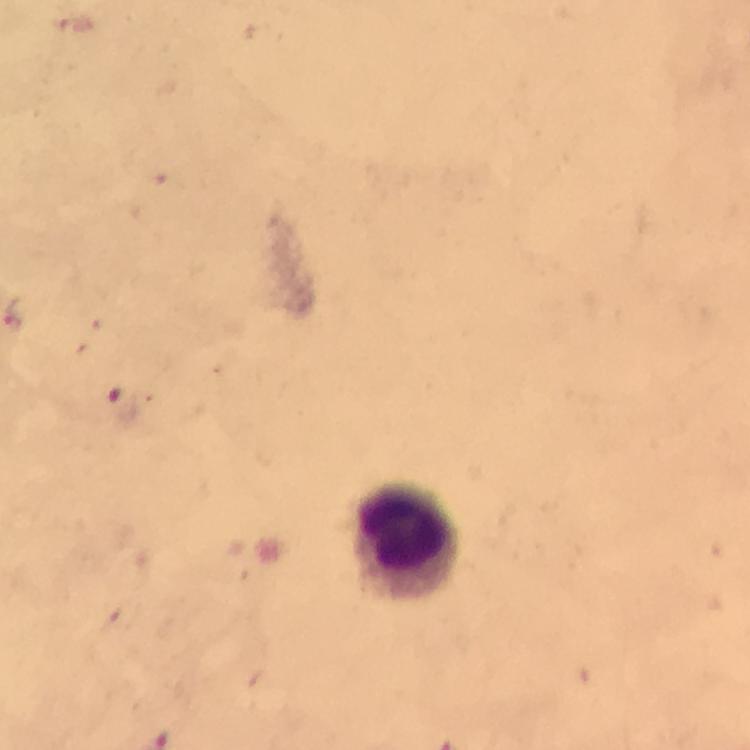
Approximate object centers, in pixels from the top-left corner. Leukocyte locations: (x=406, y=541). Malaria parasite locations: (x=124, y=404). From a diagnostic examination for malaria. At 100x magnification. Immersion oil was used. Image is 750×750 pixels. Thick blood smear. A crop from one field of view. Photographed through the microscope with a smartphone camera. Giemsa-stained preparation.